Locate and identify every blood parasite.
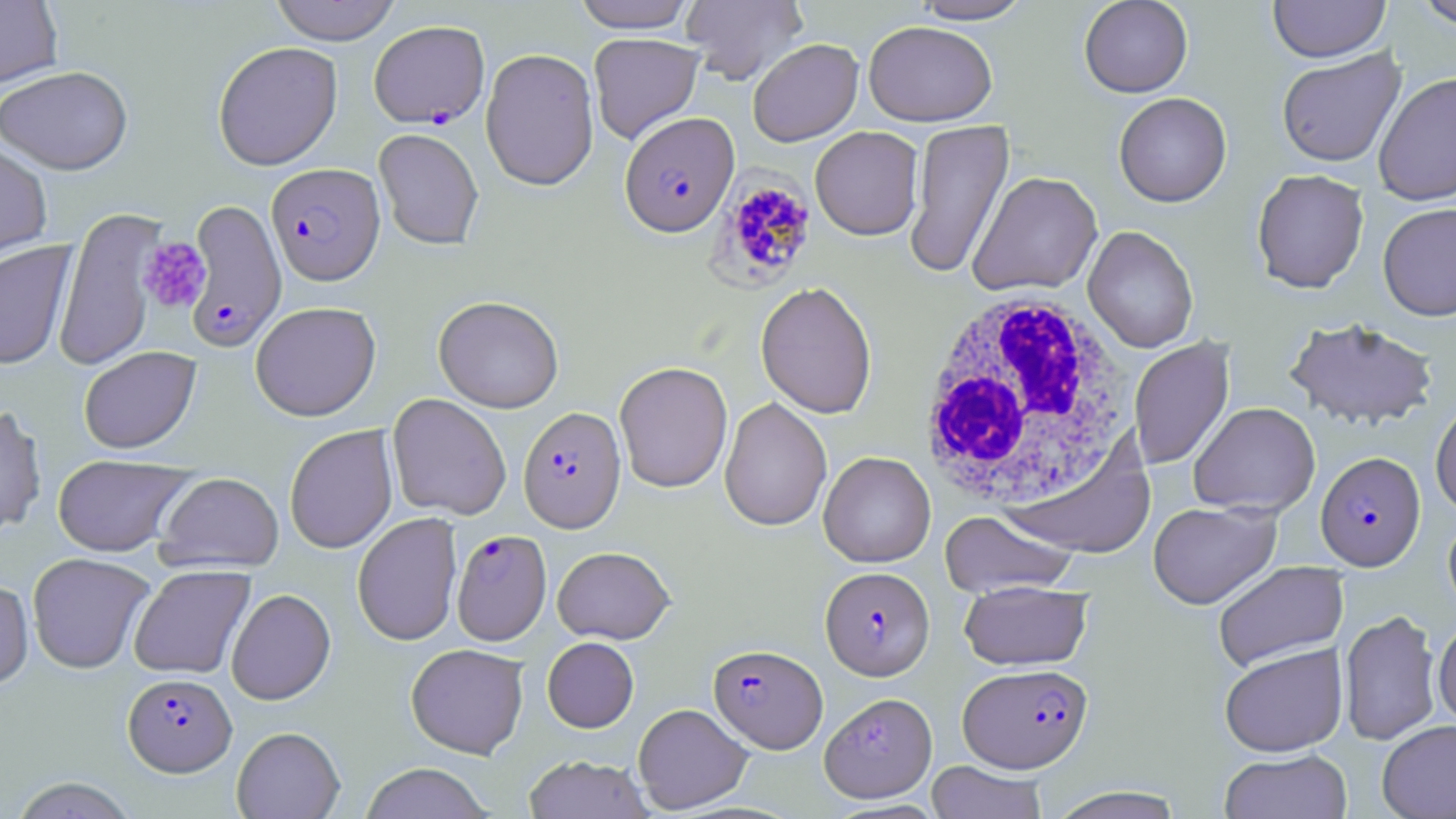
Approximate bounding boxes as (x1, y1, x2, y2) in pixels.
Plasmodium falciparum-infected red blood cells: (369, 20, 489, 128), (619, 112, 739, 236), (266, 163, 385, 285), (711, 165, 818, 287), (184, 199, 288, 352), (518, 406, 626, 532), (1316, 451, 1425, 570), (452, 529, 551, 645), (820, 566, 934, 680), (708, 644, 827, 752), (958, 662, 1093, 773), (123, 672, 236, 776).
No Plasmodium ovale, Plasmodium malariae, Plasmodium vivax, Babesia divergens, or Trypanosoma brucei observed.

slide-level diagnosis = Plasmodium falciparum
white blood cell locations = approximate bounding boxes as (x1, y1, x2, y2) in pixels: (914, 289, 1132, 513)
stain = May-Grünwald-Giemsa
preparation = thin blood film
image size = 1456×819 pixels
uninfected red blood cell locations = approximate bounding boxes as (x1, y1, x2, y2) in pixels: (0, 0, 63, 87), (269, 0, 402, 45), (680, 0, 807, 85), (911, 0, 1034, 24), (1079, 0, 1193, 97), (1414, 0, 1456, 30), (572, 1, 698, 33), (1268, 1, 1390, 62), (863, 20, 997, 126), (588, 33, 705, 145), (748, 38, 863, 146), (213, 41, 343, 170), (481, 48, 599, 191), (1277, 49, 1406, 167), (0, 65, 133, 175), (1374, 72, 1456, 206), (1114, 92, 1232, 208), (904, 119, 1014, 279), (810, 126, 923, 240), (373, 128, 484, 250), (0, 140, 53, 263), (1251, 169, 1369, 294), (968, 171, 1102, 297), (1378, 202, 1456, 321), (53, 207, 164, 372), (1083, 225, 1199, 353), (0, 240, 76, 370), (755, 281, 877, 419), (434, 295, 563, 413), (250, 301, 381, 420), (1284, 316, 1439, 431), (1128, 338, 1235, 470), (78, 347, 200, 454), (614, 361, 733, 493), (387, 393, 511, 520), (720, 397, 832, 532), (1430, 398, 1456, 517), (1189, 402, 1320, 518), (0, 404, 47, 536), (284, 425, 398, 554), (1000, 434, 1157, 560), (818, 450, 936, 567), (52, 454, 194, 557), (155, 471, 284, 572), (1148, 502, 1280, 608), (940, 509, 1079, 599), (352, 513, 462, 646), (1443, 513, 1456, 620), (552, 546, 675, 644), (27, 552, 154, 674), (1212, 561, 1348, 671), (129, 565, 254, 679), (0, 578, 34, 690), (959, 581, 1092, 671), (226, 588, 336, 705), (1339, 609, 1442, 746), (1432, 619, 1456, 727), (542, 637, 639, 732), (405, 643, 529, 759), (1219, 643, 1347, 757), (820, 692, 937, 802), (633, 703, 753, 813), (1377, 720, 1456, 819), (231, 726, 345, 818), (1219, 749, 1353, 819), (523, 754, 653, 818), (925, 761, 1048, 819), (358, 763, 494, 819), (8, 776, 140, 819), (1047, 786, 1187, 819)
field of view = single
magnification = 1000x
modality = light microscopy
platelet locations = approximate bounding boxes as (x1, y1, x2, y2) in pixels: (137, 238, 211, 313)